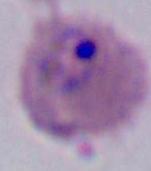

Summary:
  - Modality: micrograph
  - Magnification: 400x or 1000x
  - Identification: Plasmodium